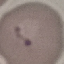
Summary:
  - Result: malaria parasites detected
  - Preparation: thin blood smear
  - Capture: smartphone camera at the microscope eyepiece
  - Image type: cell patch, automatically extracted from a larger field of view and resized to 64 × 64 pixels
  - Stain: Giemsa